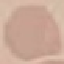 Malaria status: uninfected. Thin blood film. Automatically extracted cell patch, resized to 64 × 64 pixels. Giemsa-stained preparation. Photographed with a smartphone camera at the microscope eyepiece.